Locate every uninfected red blood cell.
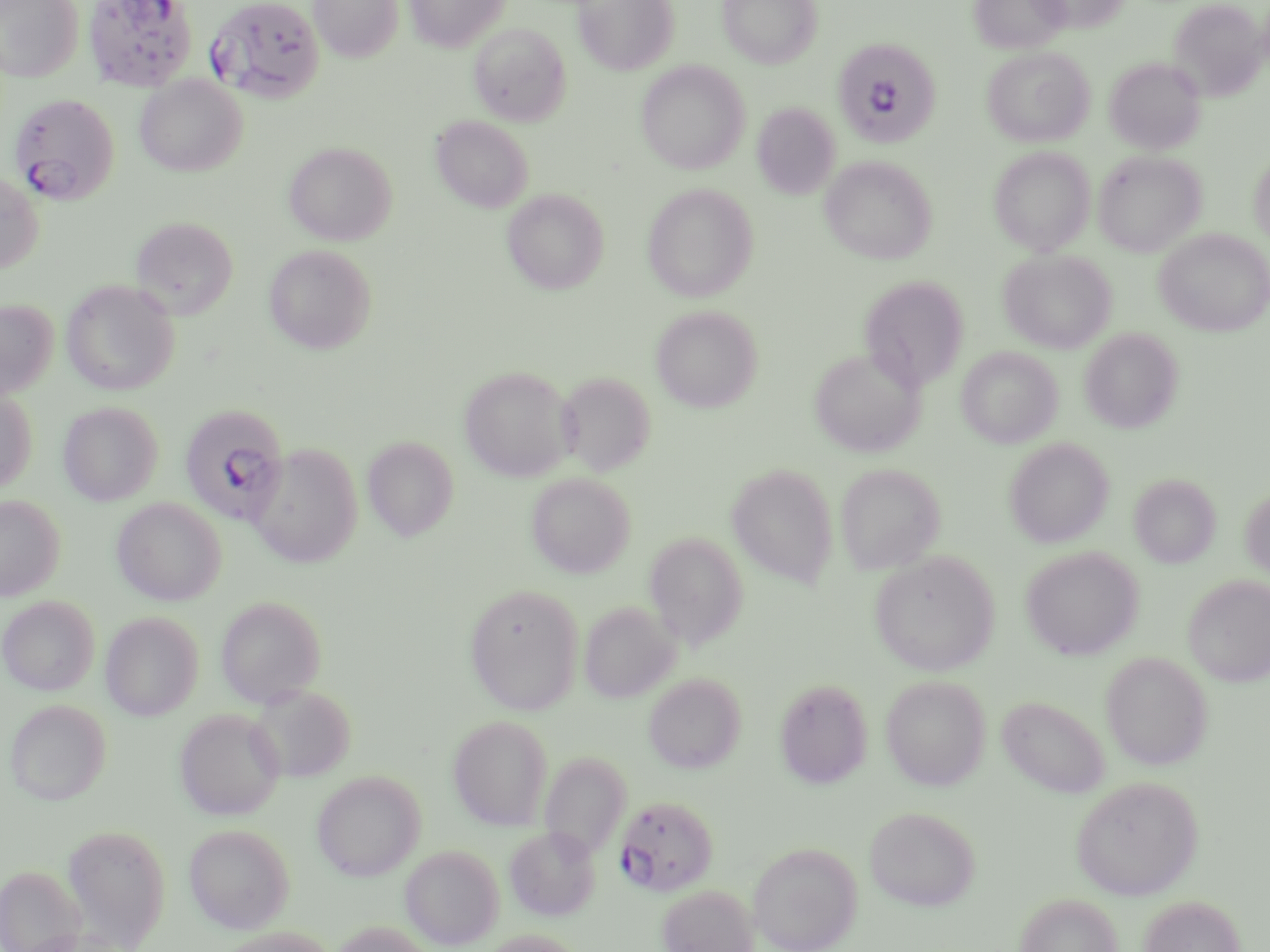

Approximate bounding boxes as [x1, y1, x2, y2] in pixels.
Uninfected red blood cells: [0, 0, 83, 82], [309, 0, 404, 62], [405, 0, 509, 52], [573, 0, 679, 75], [718, 0, 823, 68], [970, 0, 1069, 54], [1029, 0, 1129, 32], [1168, 0, 1268, 99], [469, 23, 571, 127], [982, 46, 1094, 147], [1104, 56, 1206, 155], [636, 61, 749, 173], [135, 75, 247, 176], [752, 102, 840, 200], [431, 115, 533, 213], [283, 141, 397, 245], [989, 146, 1095, 255], [1248, 149, 1270, 251], [1094, 150, 1206, 256], [820, 155, 937, 264], [0, 170, 43, 274], [642, 183, 759, 301], [502, 188, 609, 294], [129, 215, 239, 320], [1154, 229, 1270, 337], [264, 244, 376, 354], [999, 249, 1116, 353], [859, 276, 969, 391], [61, 279, 180, 395], [0, 299, 58, 400], [651, 305, 762, 413], [1079, 327, 1183, 433], [957, 346, 1063, 448], [810, 348, 926, 458], [459, 366, 574, 482], [557, 371, 657, 476], [0, 389, 37, 494], [58, 402, 162, 506], [362, 436, 460, 541], [1004, 437, 1114, 548], [248, 443, 362, 568], [835, 463, 946, 574], [727, 464, 838, 587], [526, 472, 636, 578], [1129, 473, 1221, 567], [1240, 485, 1270, 581], [0, 494, 65, 601], [112, 497, 227, 605], [644, 532, 748, 649], [1021, 547, 1143, 660], [869, 551, 1000, 676], [1183, 574, 1270, 687], [465, 583, 584, 714], [0, 595, 100, 695], [216, 596, 327, 708], [579, 601, 680, 703], [1, 603, 201, 703], [100, 611, 203, 720], [1100, 652, 1213, 770], [643, 673, 745, 773], [880, 675, 990, 790], [774, 678, 873, 789], [249, 684, 356, 782], [998, 695, 1111, 798], [5, 699, 111, 805], [174, 709, 286, 820], [448, 714, 553, 830], [539, 751, 631, 859], [312, 770, 426, 881], [1070, 774, 1204, 900], [865, 806, 980, 911], [183, 822, 295, 933], [61, 823, 171, 950], [506, 825, 600, 922], [748, 841, 862, 952], [401, 845, 503, 949], [0, 864, 87, 952], [657, 883, 759, 952], [1015, 892, 1123, 952], [1138, 895, 1246, 952], [211, 926, 338, 952], [478, 929, 585, 952].

{
  "slide_level_diagnosis": "Plasmodium falciparum",
  "stain": "May-Grünwald-Giemsa",
  "image_size": "1270×952 pixels",
  "field_of_view": "one of a larger specimen",
  "magnification": "1000x",
  "preparation": "thin blood film",
  "plasmodium_falciparum_infected_red_blood_cell_locations": "approximate bounding boxes as [x1, y1, x2, y2] in pixels: [84, 0, 199, 90], [206, 0, 325, 102], [835, 37, 953, 158], [9, 92, 120, 205], [180, 405, 289, 523], [614, 794, 719, 896]",
  "modality": "optical microscopy"
}